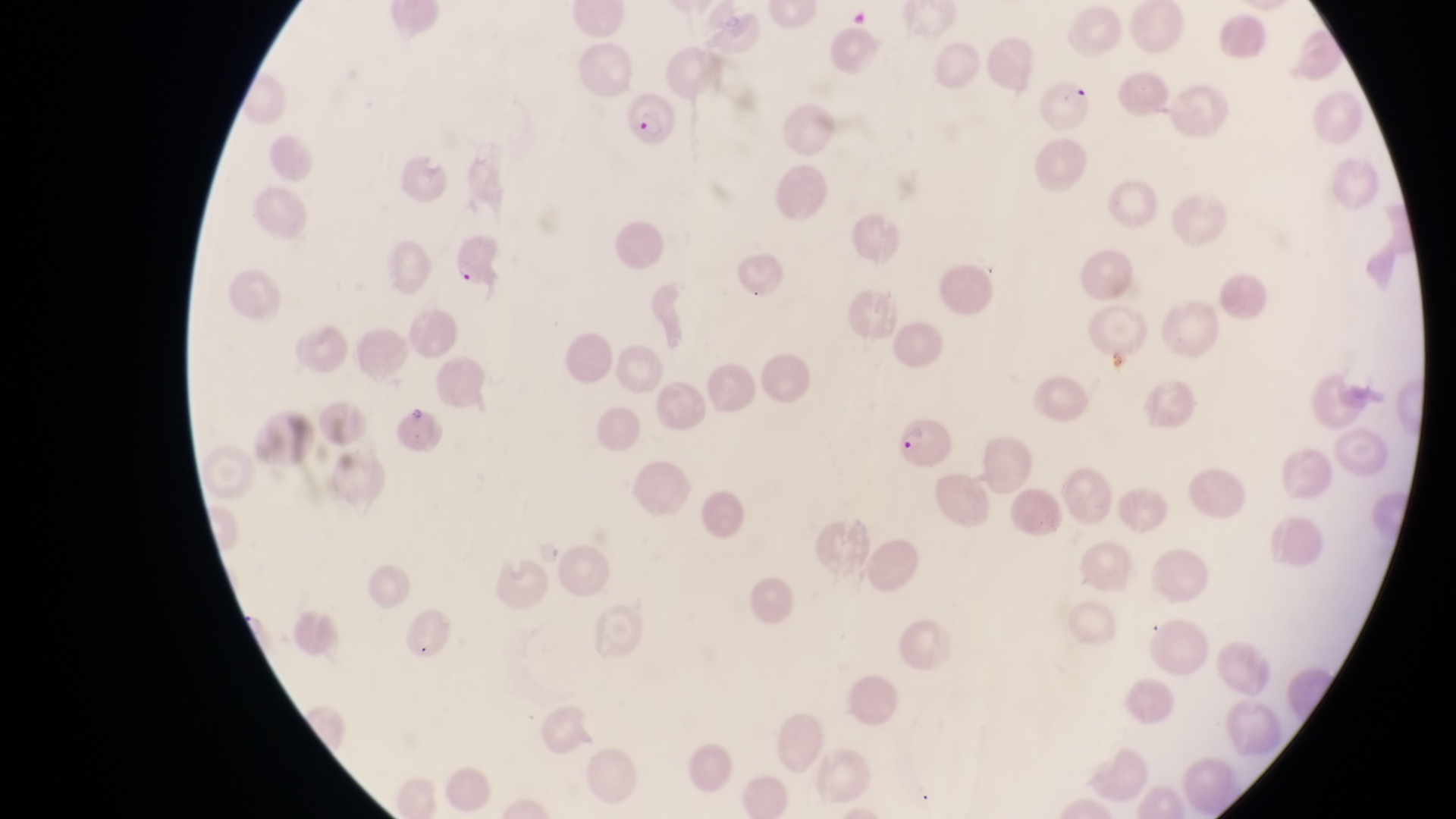

magnification = 1000x
capture = smartphone photograph through the eyepiece of an Olympus CX-23 microscope
preparation = thin blood film
country = Uganda
parasitised red blood cell locations = approximate bounding boxes as {left, top, right, bottom} in pixels: {1040, 72, 1098, 131}, {627, 93, 680, 157}, {450, 231, 511, 292}, {893, 413, 954, 465}
field of view = single
image size = 1456×819 pixels